Locate every blood parasite and identify its species.
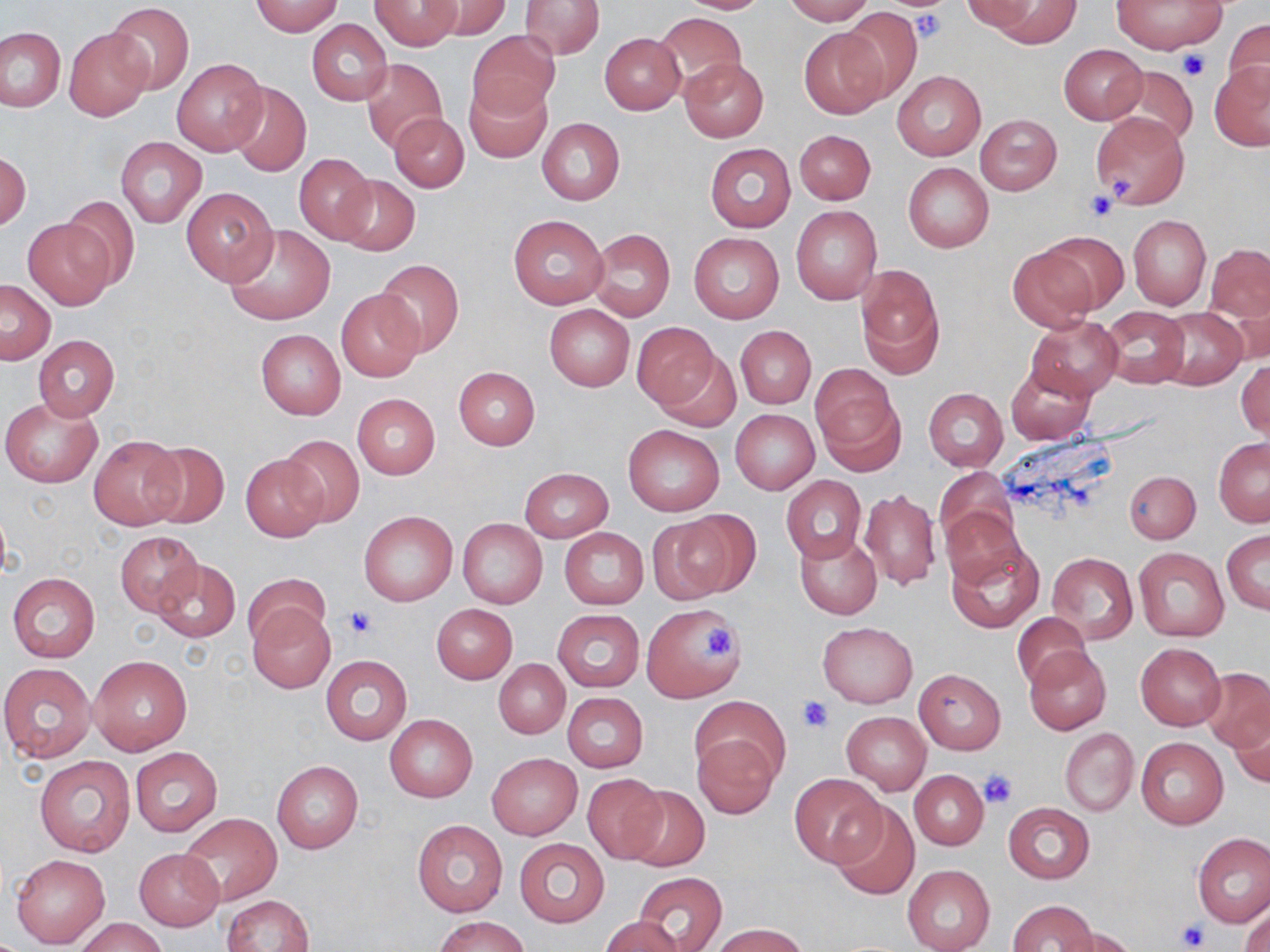
No blood parasites seen.

slide-level diagnosis = no evidence of blood parasites
modality = light microscopy
uninfected red blood cell locations = approximate bounding boxes as [x1, y1, x2, y2] in pixels: [370, 0, 465, 49], [425, 0, 512, 40], [673, 0, 773, 14], [783, 0, 873, 25], [987, 0, 1080, 47], [1113, 0, 1224, 54], [252, 1, 344, 36], [520, 1, 605, 59], [963, 1, 1039, 35], [106, 3, 193, 94], [840, 8, 922, 105], [654, 12, 747, 94], [1222, 18, 1270, 104], [306, 19, 393, 106], [0, 27, 65, 111], [65, 27, 153, 120], [798, 28, 890, 119], [468, 30, 560, 122], [599, 32, 686, 115], [1059, 44, 1147, 124], [171, 58, 268, 156], [360, 58, 448, 153], [679, 58, 768, 141], [1209, 62, 1270, 150], [1111, 66, 1198, 150], [893, 70, 986, 161], [227, 81, 311, 176], [465, 81, 551, 163], [1090, 111, 1190, 208], [390, 112, 469, 192], [975, 113, 1061, 195], [536, 118, 625, 204], [794, 129, 876, 204], [116, 136, 206, 228], [704, 144, 796, 232], [1, 152, 31, 232], [293, 153, 377, 245], [903, 163, 993, 252], [335, 175, 421, 256], [181, 186, 279, 285], [62, 195, 140, 291], [790, 205, 883, 306], [1128, 213, 1210, 310], [509, 214, 609, 309], [23, 217, 115, 310], [225, 224, 335, 325], [588, 228, 675, 321], [688, 231, 784, 324], [1040, 231, 1129, 314], [1206, 243, 1270, 323], [1007, 244, 1099, 334], [375, 259, 464, 357], [855, 262, 945, 376], [1, 280, 56, 363], [337, 291, 424, 382], [544, 304, 635, 390], [1100, 306, 1190, 388], [1153, 306, 1248, 390], [1027, 314, 1124, 399], [631, 321, 719, 410], [735, 325, 816, 409], [256, 329, 346, 420], [32, 336, 120, 420], [654, 345, 742, 432], [1236, 358, 1270, 440], [1006, 361, 1097, 445], [812, 365, 903, 473], [453, 366, 541, 450], [923, 388, 1008, 471], [352, 394, 440, 479], [1, 398, 102, 487], [730, 408, 819, 494], [622, 424, 723, 515], [87, 432, 187, 531], [278, 434, 366, 527], [1213, 437, 1270, 526], [141, 439, 229, 527], [241, 455, 328, 541], [934, 467, 1015, 551], [519, 468, 614, 542], [1125, 470, 1200, 543], [779, 475, 866, 565], [859, 487, 942, 590], [942, 502, 1024, 591], [359, 510, 458, 606], [647, 516, 740, 604], [457, 518, 548, 609], [559, 527, 648, 609], [795, 530, 882, 619], [1221, 530, 1270, 613], [115, 531, 202, 615], [945, 534, 1044, 633], [1133, 546, 1229, 641], [1046, 552, 1137, 645], [150, 558, 239, 643], [243, 572, 329, 648], [7, 573, 100, 663], [640, 603, 746, 703], [248, 604, 334, 693], [432, 604, 518, 683], [553, 610, 644, 692], [1013, 612, 1090, 691], [818, 622, 917, 707], [1135, 643, 1225, 730], [1025, 647, 1111, 735], [89, 654, 192, 756], [320, 654, 412, 744], [494, 659, 570, 738], [0, 662, 95, 762], [913, 668, 1006, 754], [1200, 668, 1270, 752], [562, 692, 648, 773], [693, 694, 786, 782], [1228, 710, 1270, 788], [840, 712, 931, 795], [385, 714, 477, 802], [1060, 728, 1138, 816], [693, 733, 781, 819], [1135, 737, 1228, 828], [129, 748, 223, 836], [487, 752, 583, 840], [34, 755, 136, 857], [272, 761, 363, 853], [910, 770, 989, 850], [788, 772, 885, 867], [581, 774, 668, 864], [622, 786, 711, 873], [831, 801, 920, 901], [1004, 802, 1094, 883], [179, 813, 282, 905], [412, 819, 507, 916], [1192, 833, 1270, 926], [514, 837, 610, 928], [134, 848, 224, 929], [10, 853, 110, 948], [902, 864, 994, 951], [633, 871, 726, 952], [221, 894, 313, 952], [1009, 900, 1097, 952], [1240, 907, 1270, 952], [601, 915, 683, 951], [435, 916, 527, 952], [75, 917, 167, 952], [712, 922, 807, 952], [1064, 929, 1138, 952]
image size = 1270×952 pixels
preparation = thin blood film
platelet locations = approximate bounding boxes as [x1, y1, x2, y2] in pixels: [911, 10, 944, 43], [1178, 48, 1210, 82], [1109, 172, 1132, 197], [1084, 190, 1117, 222], [345, 606, 378, 640], [701, 627, 735, 658], [799, 697, 831, 733], [979, 769, 1017, 807], [1177, 921, 1209, 950]
magnification = 1000x
field of view = single
stain = May-Grünwald-Giemsa